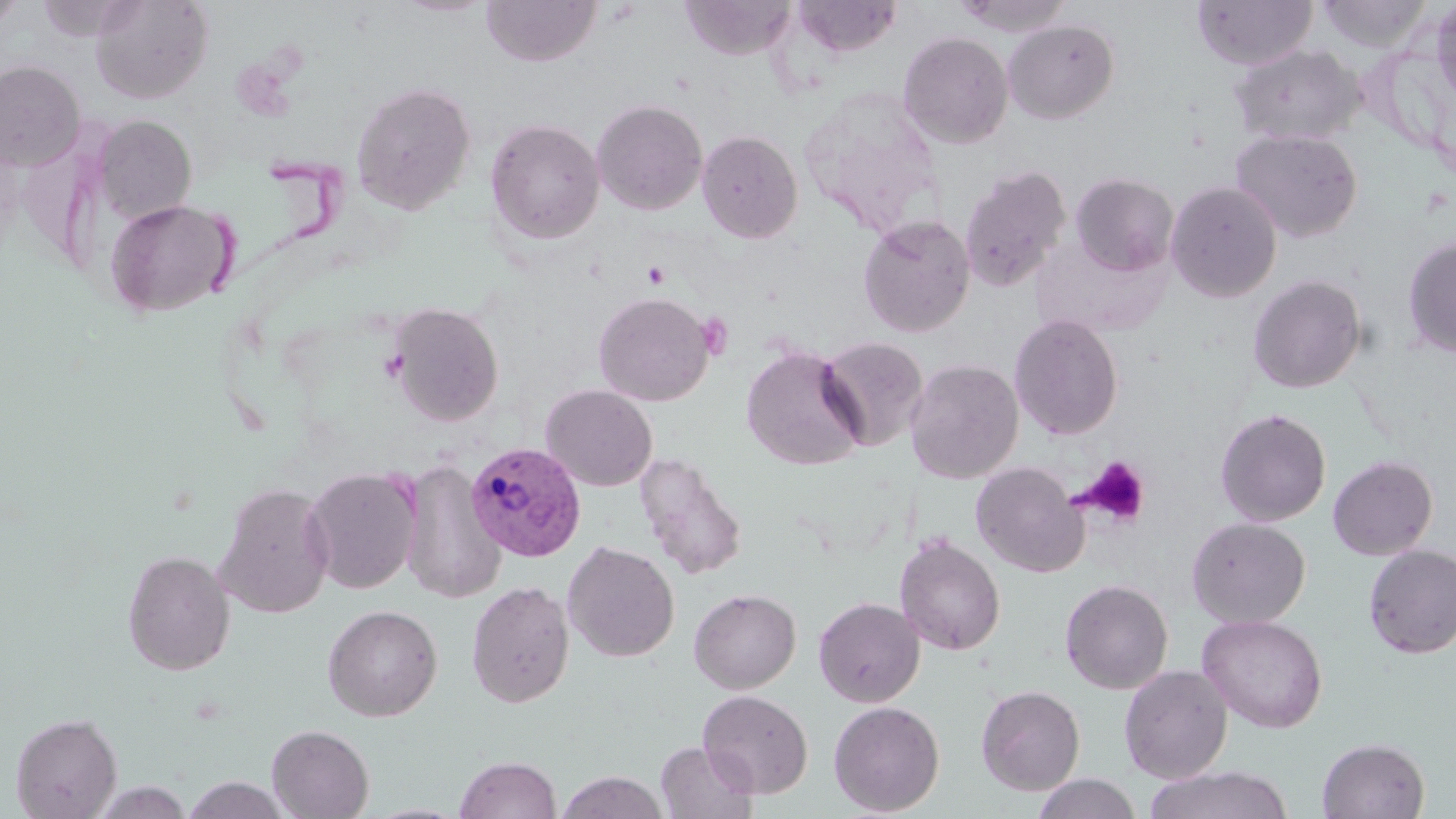

Approximate bounding boxes as (x1, y1, x2, y2) in pixels. Plasmodium vivax-infected red blood cell locations: (466, 441, 586, 562). Uninfected red blood cell locations: (0, 0, 28, 31), (89, 0, 213, 104), (481, 0, 602, 67), (680, 0, 798, 61), (793, 0, 903, 58), (953, 0, 1075, 37), (1192, 0, 1317, 70), (1430, 0, 1456, 109), (1316, 1, 1432, 51), (1003, 19, 1120, 124), (897, 31, 1013, 148), (1228, 43, 1364, 147), (0, 60, 86, 171), (351, 81, 476, 215), (797, 89, 946, 236), (591, 98, 708, 215), (93, 115, 197, 223), (485, 118, 605, 245), (1230, 128, 1363, 242), (697, 129, 804, 243), (958, 165, 1072, 292), (1070, 172, 1179, 276), (1166, 181, 1283, 302), (105, 199, 236, 318), (857, 214, 976, 338), (1402, 234, 1456, 358), (1248, 274, 1367, 394), (593, 291, 714, 406), (386, 301, 504, 426), (1009, 314, 1123, 441), (816, 335, 929, 452), (740, 346, 867, 470), (905, 358, 1024, 483), (540, 384, 658, 491), (1214, 407, 1331, 526), (635, 453, 747, 580), (1327, 455, 1438, 560), (397, 458, 505, 604), (971, 461, 1088, 577), (303, 466, 422, 594), (213, 482, 336, 619), (1187, 517, 1310, 628), (895, 534, 1006, 656), (562, 540, 680, 662), (1363, 544, 1456, 658), (121, 549, 235, 675), (1059, 579, 1174, 694), (466, 580, 575, 708), (688, 588, 801, 694), (813, 596, 925, 707), (322, 604, 442, 721), (1197, 613, 1328, 733), (1119, 664, 1233, 783), (976, 684, 1085, 795), (698, 689, 813, 798), (828, 700, 946, 816), (10, 711, 122, 819), (267, 724, 374, 819), (1317, 737, 1430, 819), (655, 741, 758, 819), (455, 755, 560, 818), (1143, 765, 1295, 819), (557, 771, 670, 819), (1032, 773, 1143, 819), (181, 775, 291, 819), (91, 780, 194, 818). Platelet locations: (642, 262, 672, 289), (696, 312, 734, 359), (1077, 456, 1150, 527). Slide-level diagnosis: Plasmodium vivax. Optical microscopy. Thin blood film. May-Grünwald-Giemsa stain. Image is 1456×819 pixels. One field of a larger specimen. 1000x magnification.